Assess for Plasmodium parasites.
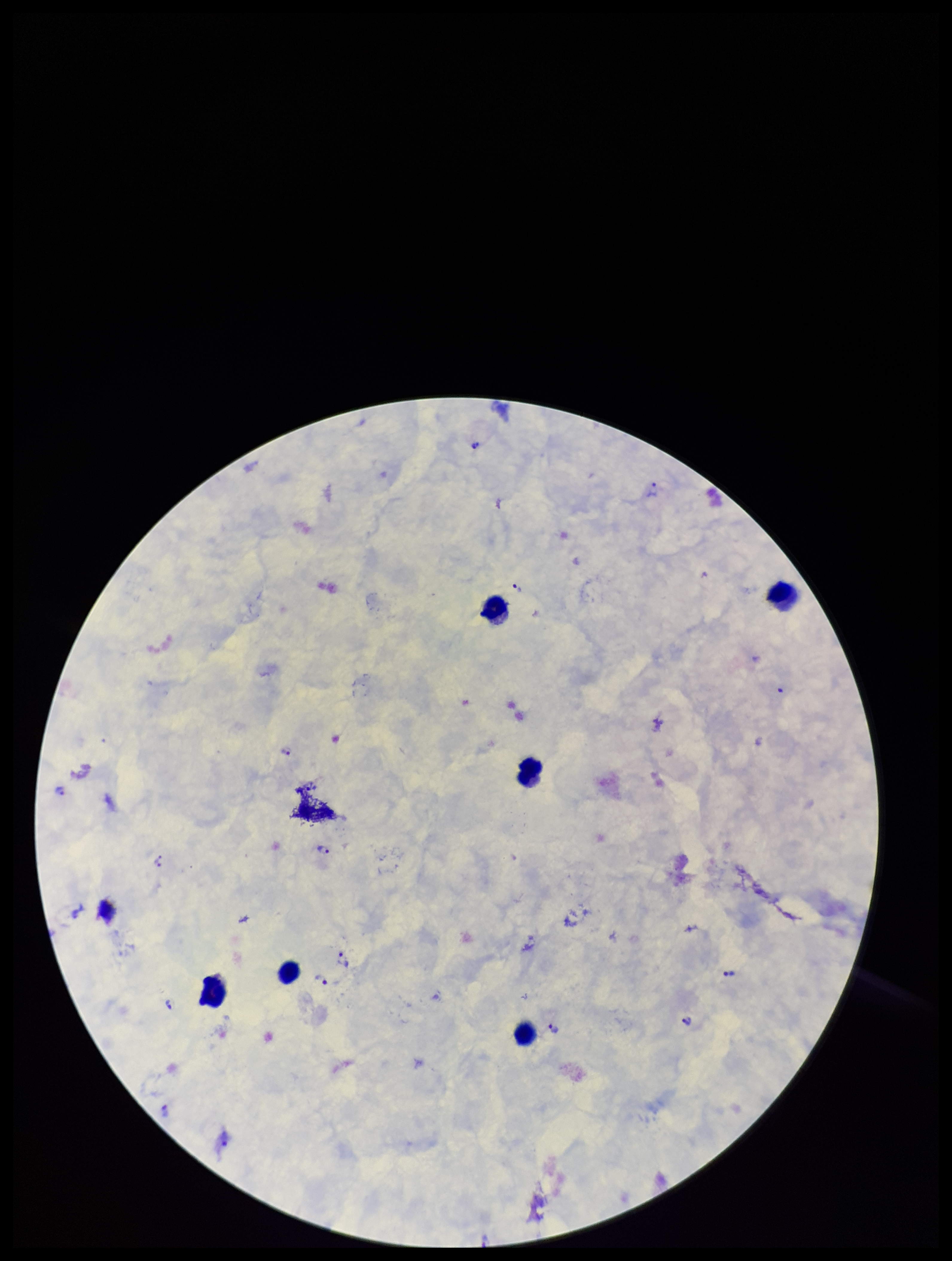
Detected.

Image is 952×1261 pixels. Patient malaria status: positive. Parasite count: 15. Leukocyte count: 6. One field from this slide. Species reported for this patient: Plasmodium vivax. Preparation: thick blood smear. Stained with Giemsa. Photographed through the microscope eyepiece with a smartphone camera.